Comment on the morphology of the red blood cells.
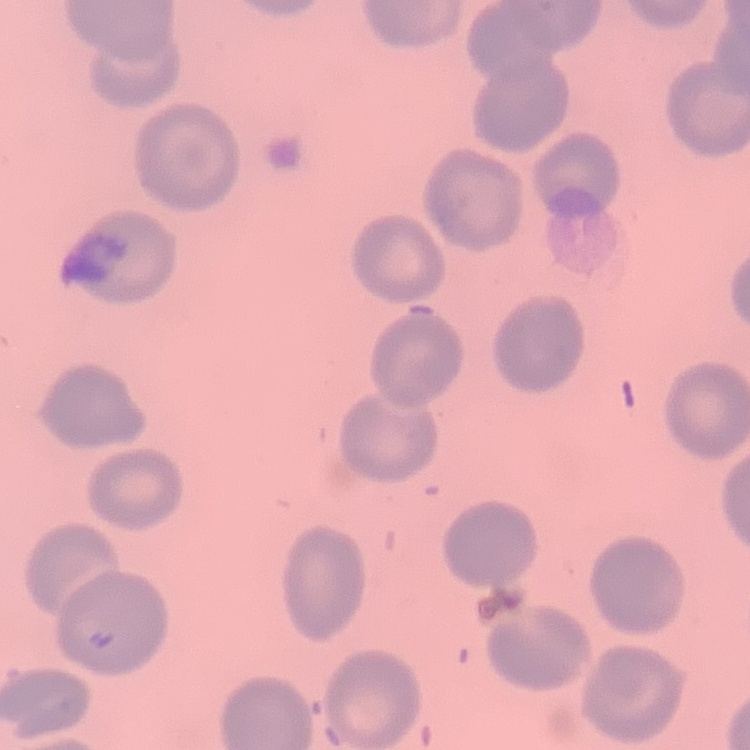
No rouleaux formation.

image type = square crop of a larger photomicrograph
preparation = thin peripheral smear
stain = Field's or Giemsa